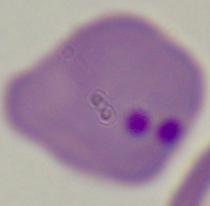

A Babesia parasite is seen. 1000x magnification. Photomicrograph.